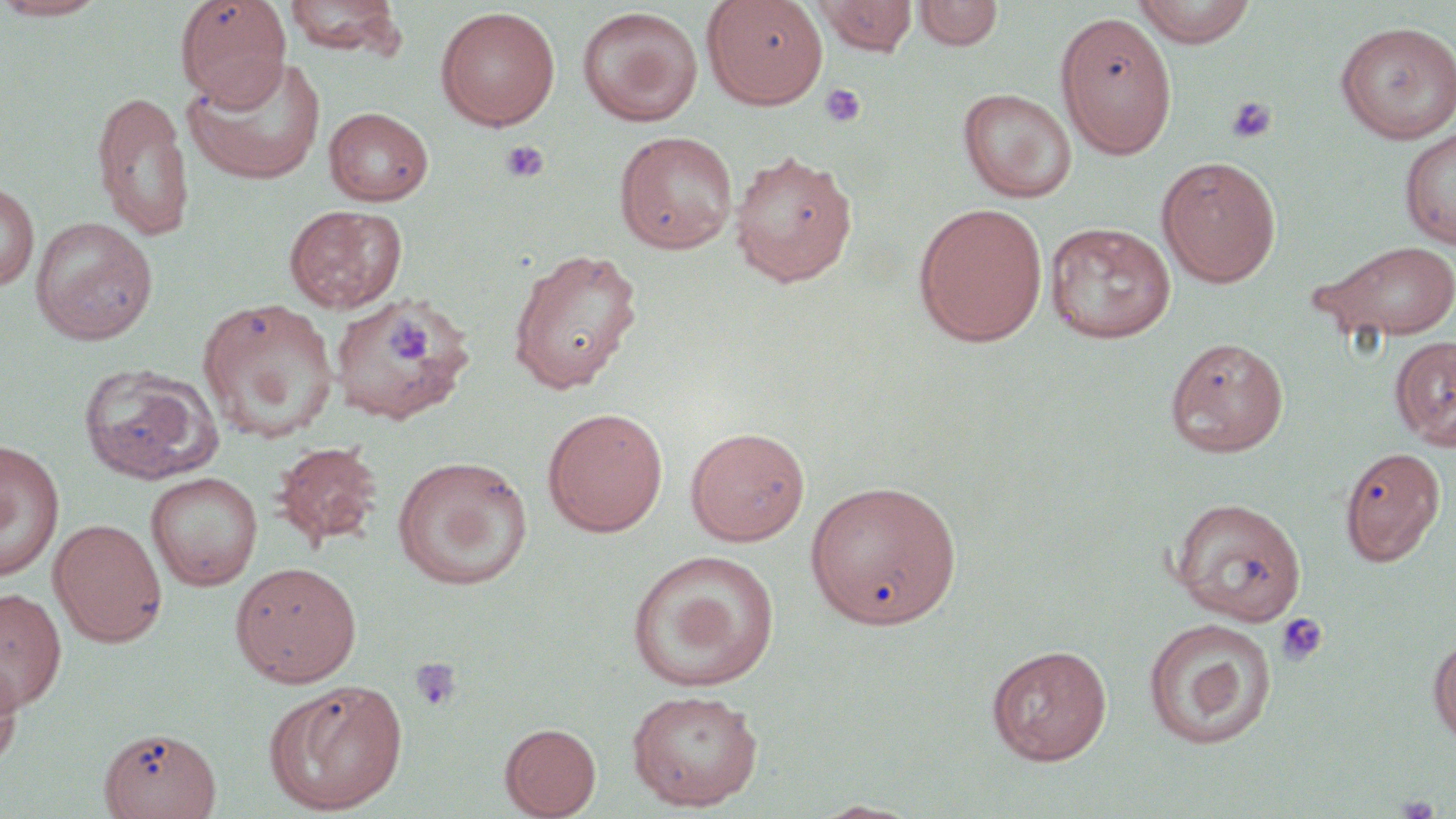

{
  "slide_level_diagnosis": "negative for blood parasites",
  "platelet_locations": "approximate bounding boxes as [x1, y1, x2, y2] in pixels: [820, 83, 866, 127], [1226, 95, 1277, 145], [500, 140, 549, 184], [385, 317, 434, 366], [1275, 612, 1330, 667], [409, 656, 462, 712]",
  "modality": "light microscopy",
  "magnification": "1000x",
  "uninfected_red_blood_cell_locations": "approximate bounding boxes as [x1, y1, x2, y2] in pixels: [0, 0, 113, 22], [175, 0, 291, 108], [282, 0, 406, 58], [702, 0, 828, 110], [812, 0, 918, 56], [913, 0, 1002, 52], [1132, 0, 1257, 47], [434, 6, 561, 130], [576, 6, 703, 127], [1055, 11, 1177, 158], [1334, 20, 1456, 144], [182, 56, 327, 185], [957, 88, 1078, 203], [91, 89, 194, 242], [323, 107, 434, 205], [1399, 126, 1456, 250], [614, 131, 738, 254], [729, 149, 858, 287], [1156, 155, 1282, 288], [0, 180, 39, 291], [913, 202, 1048, 347], [283, 204, 407, 314], [30, 216, 158, 345], [1044, 222, 1176, 344], [1308, 239, 1456, 343], [507, 246, 643, 394], [328, 293, 474, 425], [197, 298, 340, 442], [1165, 336, 1290, 457], [1389, 336, 1456, 451], [78, 363, 222, 485], [542, 407, 668, 537], [685, 426, 810, 546], [0, 440, 65, 582], [271, 440, 384, 551], [1338, 445, 1447, 567], [391, 455, 534, 591], [145, 472, 262, 590], [805, 479, 963, 631], [1170, 497, 1307, 625], [49, 518, 167, 647], [627, 549, 780, 692], [230, 561, 362, 686], [0, 586, 67, 713], [1143, 617, 1277, 749], [1428, 636, 1456, 745], [987, 644, 1112, 765], [0, 654, 23, 774], [264, 681, 408, 815], [625, 689, 764, 811], [500, 722, 602, 818], [98, 725, 222, 819], [812, 799, 923, 818]",
  "image_size": "1456×819 pixels",
  "stain": "May-Grünwald-Giemsa",
  "field_of_view": "single",
  "preparation": "thin blood film"
}